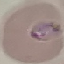
Malaria status: parasitized. Cell patch, automatically extracted from a larger field of view and resized to 64 × 64 pixels. Giemsa-stained preparation. Photographed with a smartphone camera at the microscope eyepiece. Thin blood film.